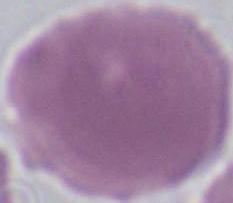

identification = erythrocyte
magnification = 1000x
modality = photomicrograph